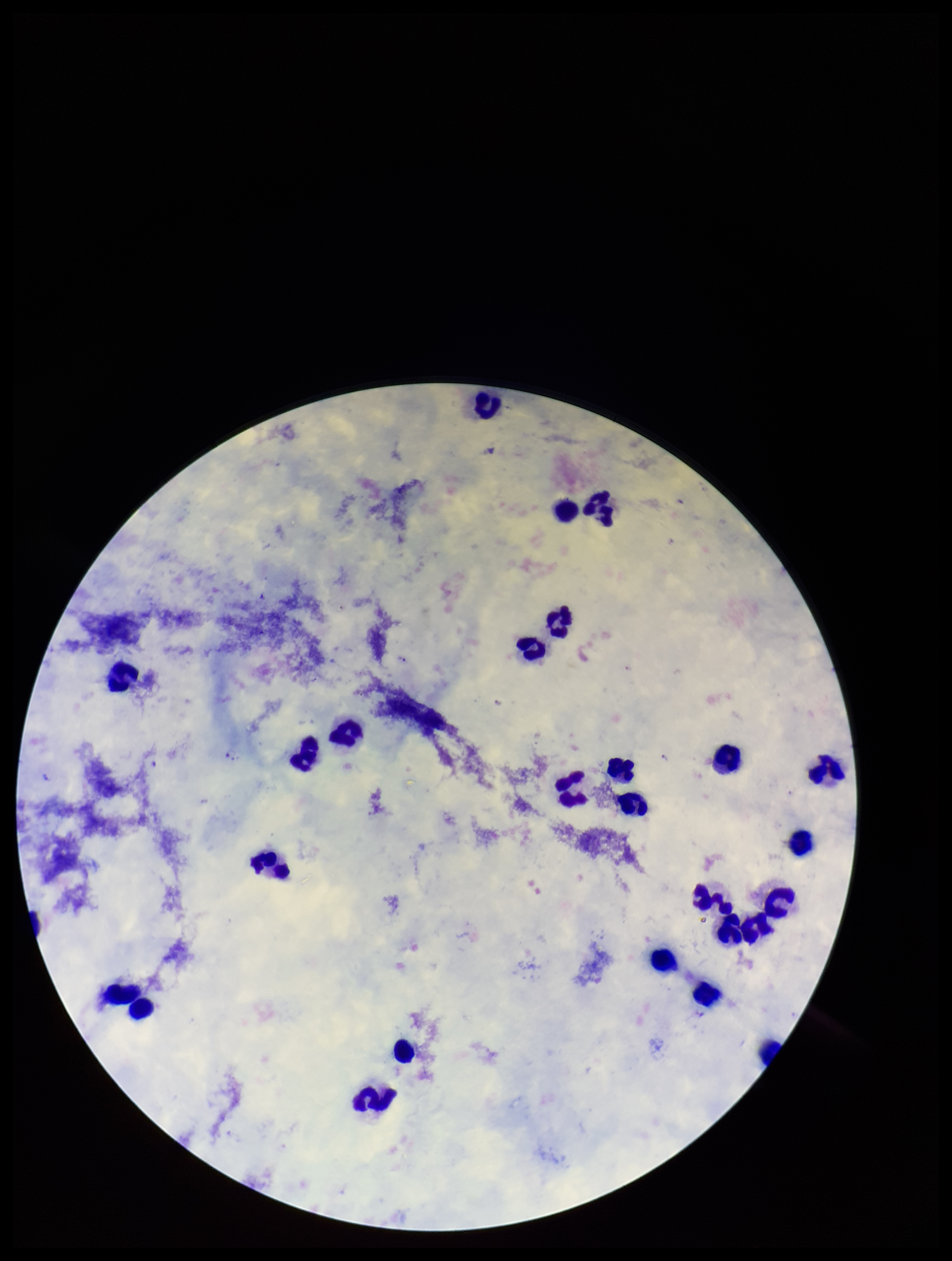
Patient malaria status: positive. Species reported for this patient: Plasmodium falciparum. Image is 952×1261 pixels. Plasmodium parasites: seen. Parasite count: 1. Smartphone photograph taken through the eyepiece of a microscope. Leukocyte count: 26. Single field of view. Preparation: thick blood smear. Giemsa stain.